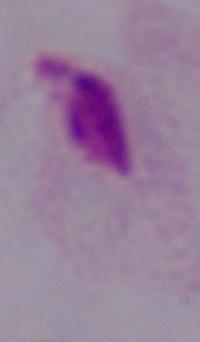

Captured at 1000x magnification. Photomicrograph. A trichomonad is shown.